Locate and identify every blood parasite.
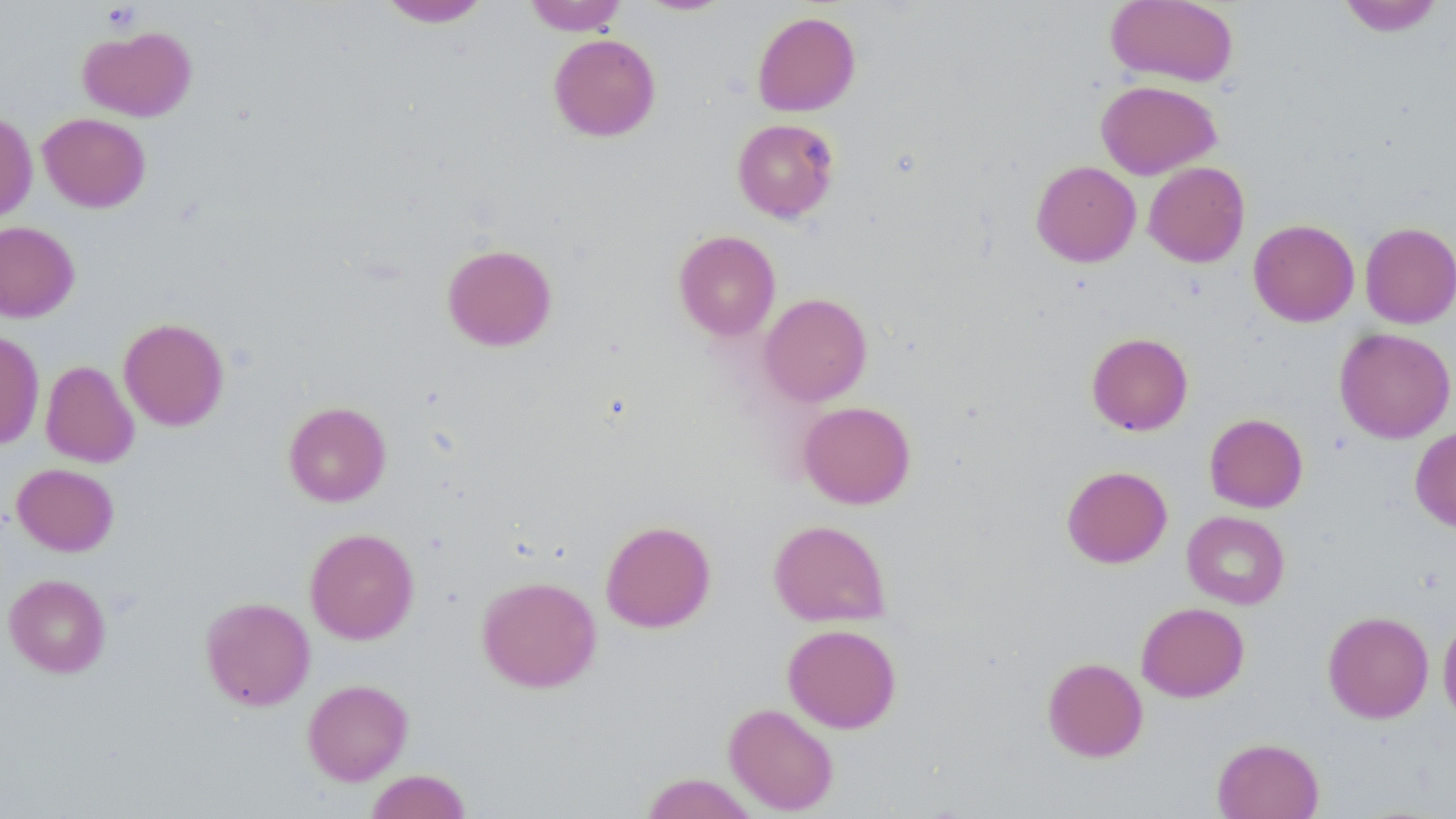

No blood parasites observed.

Approximate bounding boxes as (x1,y1)-(x2,y2) corner pairs in pixels. Uninfected red blood cell locations: (378,0)-(492,27), (524,0)-(628,35), (1105,0)-(1238,87), (1337,0)-(1445,36), (634,1)-(737,16), (752,11)-(860,116), (79,26)-(197,121), (548,33)-(661,142), (1096,79)-(1221,179), (0,112)-(38,223), (38,112)-(151,212), (732,118)-(839,222), (1031,160)-(1141,267), (1143,161)-(1250,267), (1248,219)-(1359,326), (0,221)-(80,323), (1360,222)-(1456,328), (674,230)-(780,340), (442,243)-(557,351), (759,292)-(872,406), (118,317)-(230,431), (1334,327)-(1455,443), (0,331)-(44,449), (1086,332)-(1193,435), (40,361)-(139,467), (283,401)-(391,506), (798,401)-(916,509), (1204,413)-(1308,513), (1410,426)-(1456,532), (12,463)-(119,556), (1062,465)-(1172,568), (1182,511)-(1290,609), (768,519)-(891,626), (600,520)-(716,632), (305,527)-(419,644), (4,574)-(111,677), (477,575)-(602,692), (200,596)-(315,711), (1136,601)-(1249,702), (1322,611)-(1434,723), (1438,614)-(1456,725), (782,623)-(902,733), (1042,657)-(1148,762), (302,679)-(413,785), (724,703)-(839,815), (1212,737)-(1324,819), (365,770)-(471,819), (639,772)-(759,818). Platelet locations: (101,2)-(142,33). Slide-level diagnosis: negative for blood parasites. One field of a larger specimen. Thin blood smear. 1000x magnification. May-Grünwald-Giemsa stain. Image is 1456×819 pixels. Optical microscopy.